Locate every blood parasite and identify its species.
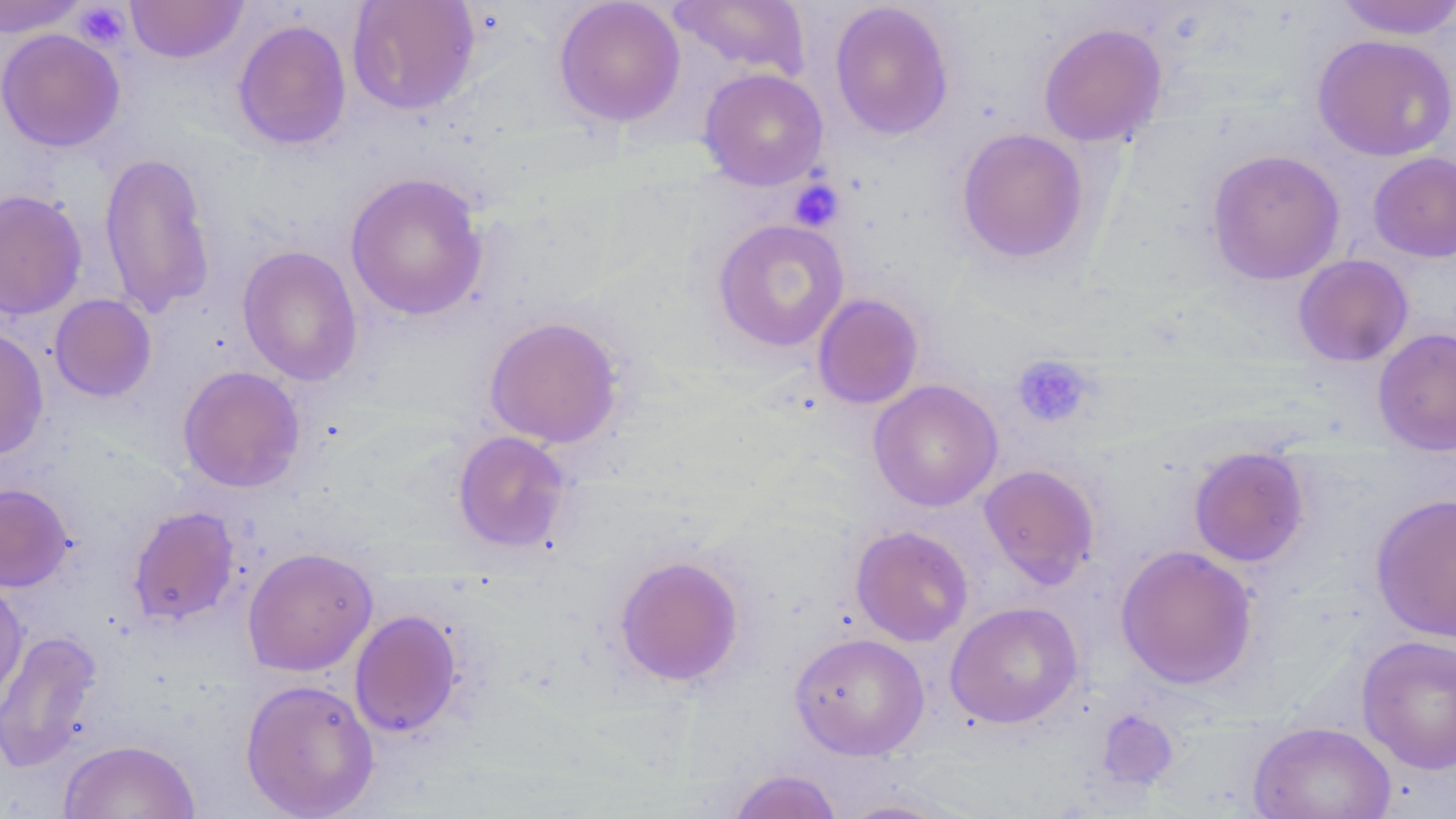

No blood parasites seen.

Summary:
  - Coordinate format: approximate bounding boxes as [x1, y1, x2, y2] in pixels
  - Uninfected red blood cell locations (subset): [125, 0, 248, 64], [347, 0, 481, 116], [553, 0, 685, 128], [668, 0, 811, 81], [1334, 0, 1456, 40], [0, 1, 88, 38], [829, 1, 954, 140], [232, 19, 352, 151], [1038, 22, 1168, 147], [0, 28, 125, 152], [1312, 34, 1456, 162], [699, 68, 829, 190], [955, 127, 1090, 265], [1206, 149, 1345, 285], [98, 151, 216, 317], [1368, 152, 1456, 262], [345, 171, 489, 321], [0, 189, 88, 320], [712, 218, 850, 352], [237, 244, 363, 386], [1292, 254, 1413, 367], [812, 293, 924, 410], [49, 294, 157, 402], [484, 315, 624, 448], [1372, 327, 1456, 455], [0, 328, 49, 461], [177, 365, 305, 493], [869, 379, 1003, 512], [452, 431, 572, 554], [1188, 446, 1310, 567], [979, 464, 1100, 588], [0, 483, 74, 592], [1370, 492, 1456, 642], [127, 505, 240, 627], [850, 525, 974, 646], [1115, 544, 1258, 690], [242, 546, 378, 677], [613, 554, 745, 687], [0, 581, 29, 714], [945, 601, 1083, 728], [349, 609, 464, 739], [1, 629, 103, 773], [790, 632, 929, 760], [1357, 634, 1456, 774], [240, 678, 379, 818], [1249, 721, 1396, 819], [58, 739, 200, 819], [726, 768, 843, 819], [833, 796, 964, 818]
  - Platelet locations (subset): [73, 3, 130, 50], [789, 179, 845, 232], [1011, 353, 1096, 429]
  - Slide-level diagnosis: no evidence of blood parasites
  - Modality: optical microscopy
  - Magnification: 1000x
  - Field of view: one of a larger specimen
  - Preparation: thin blood smear
  - Stain: May-Grünwald-Giemsa
  - Image size: 1456×819 pixels